Look for Plasmodium parasites.
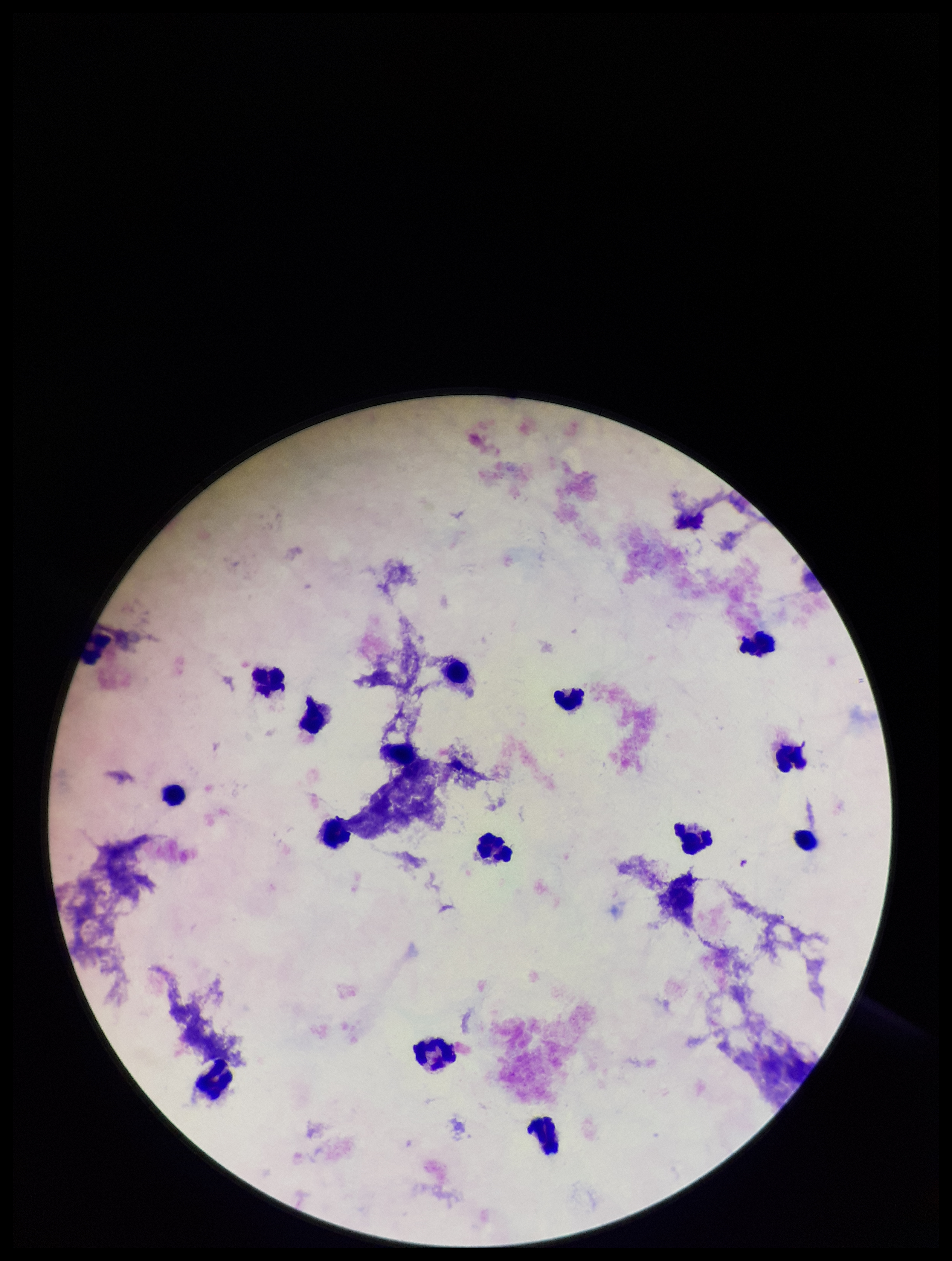
None identified.

Patient malaria status: negative. Photographed through the microscope eyepiece with a smartphone camera. Stained with Giemsa. Image is 952×1261 pixels. Leukocyte count: 14. Preparation: thick smear. One field from this slide. Parasite count: 0.